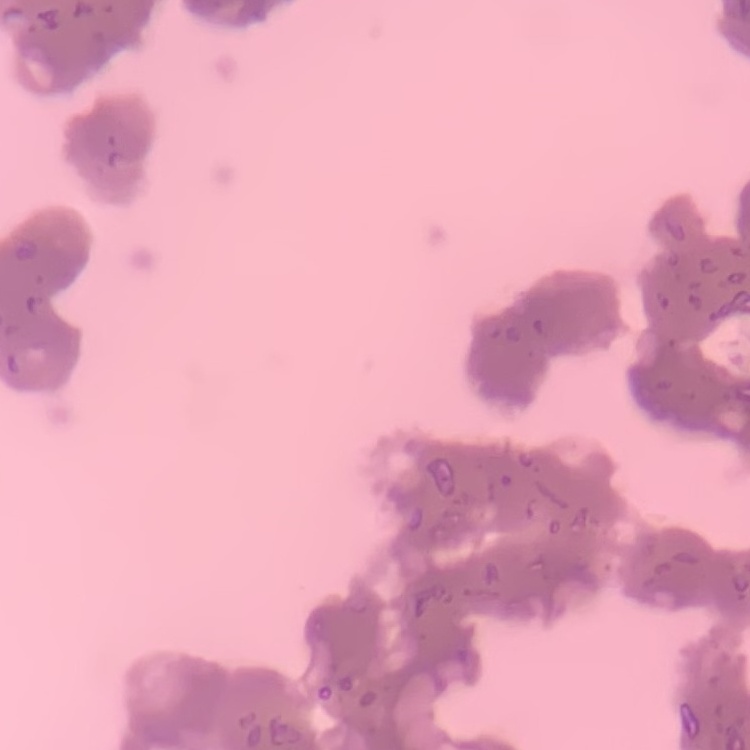
The red blood cells show rouleaux formation. Square crop of a larger photomicrograph. Field's or Giemsa stain. Thin peripheral smear.